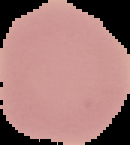
image size = 130×145 pixels
result = no Plasmodium parasites seen
image type = segmented cell region with the area outside set to black
preparation = thin blood smear